State which cell type is depicted.
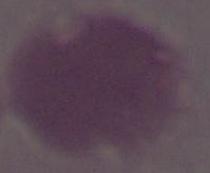
An erythrocyte.

Micrograph. Captured at 1000x magnification.